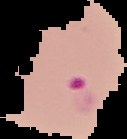

Summary:
  - Preparation: thin blood film
  - Image size: 127×139 pixels
  - Malaria status: parasitized
  - Image type: cell region segmented out of the field of view; surrounding area masked to black